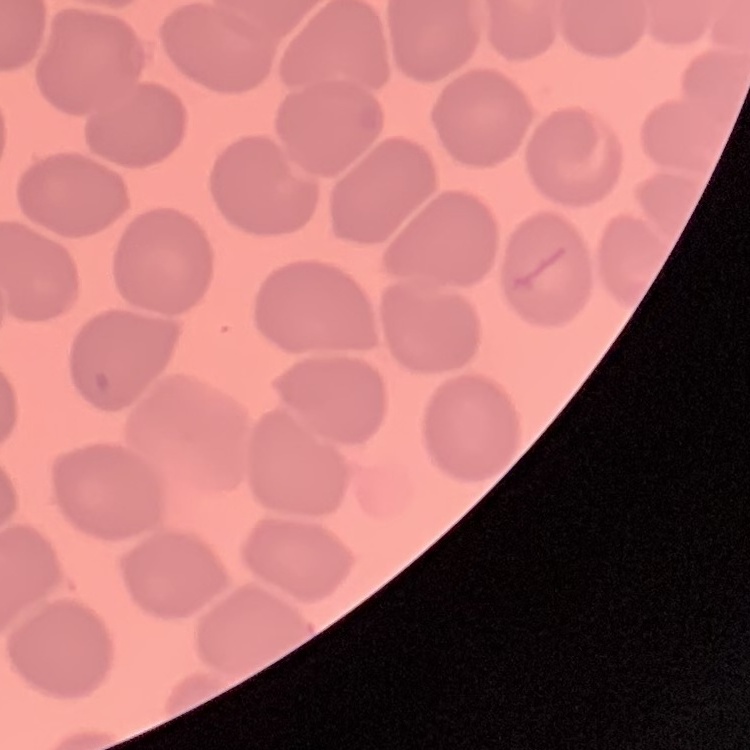
The red blood cells exhibit no rouleaux formation. Thin blood smear. Square crop of a larger photomicrograph. Field's or Giemsa stain.